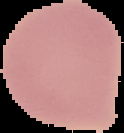
{
  "preparation": "thin blood smear",
  "malaria_status": "uninfected",
  "image_type": "segmented cell region with the area outside set to black",
  "image_size": "124×133 pixels"
}